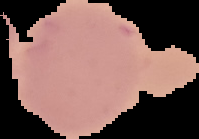
Summary:
  - Image size: 199×139 pixels
  - Image type: segmented cell region with the area outside set to black
  - Malaria status: uninfected
  - Preparation: thin blood smear